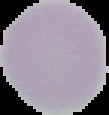
image type = cell region segmented out of the field of view; surrounding area masked to black
preparation = thin blood smear
image size = 109×115 pixels
result = negative for Plasmodium parasites